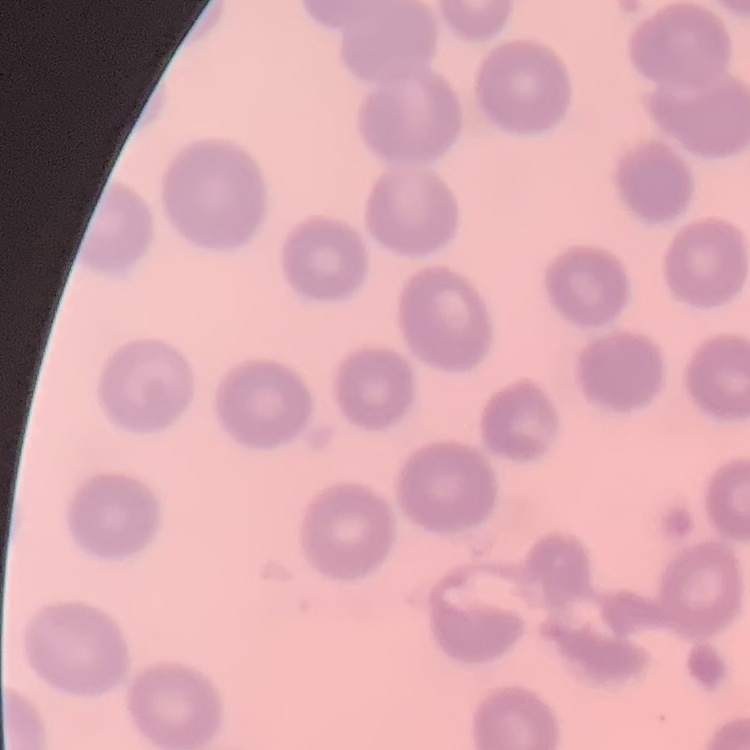

red blood cell morphology = no rouleaux formation
image type = one tile cut from a larger photomicrograph
stain = Field's or Giemsa
preparation = thin blood smear